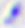
Toxoplasma gondii is shown. Micrograph. 400x magnification.